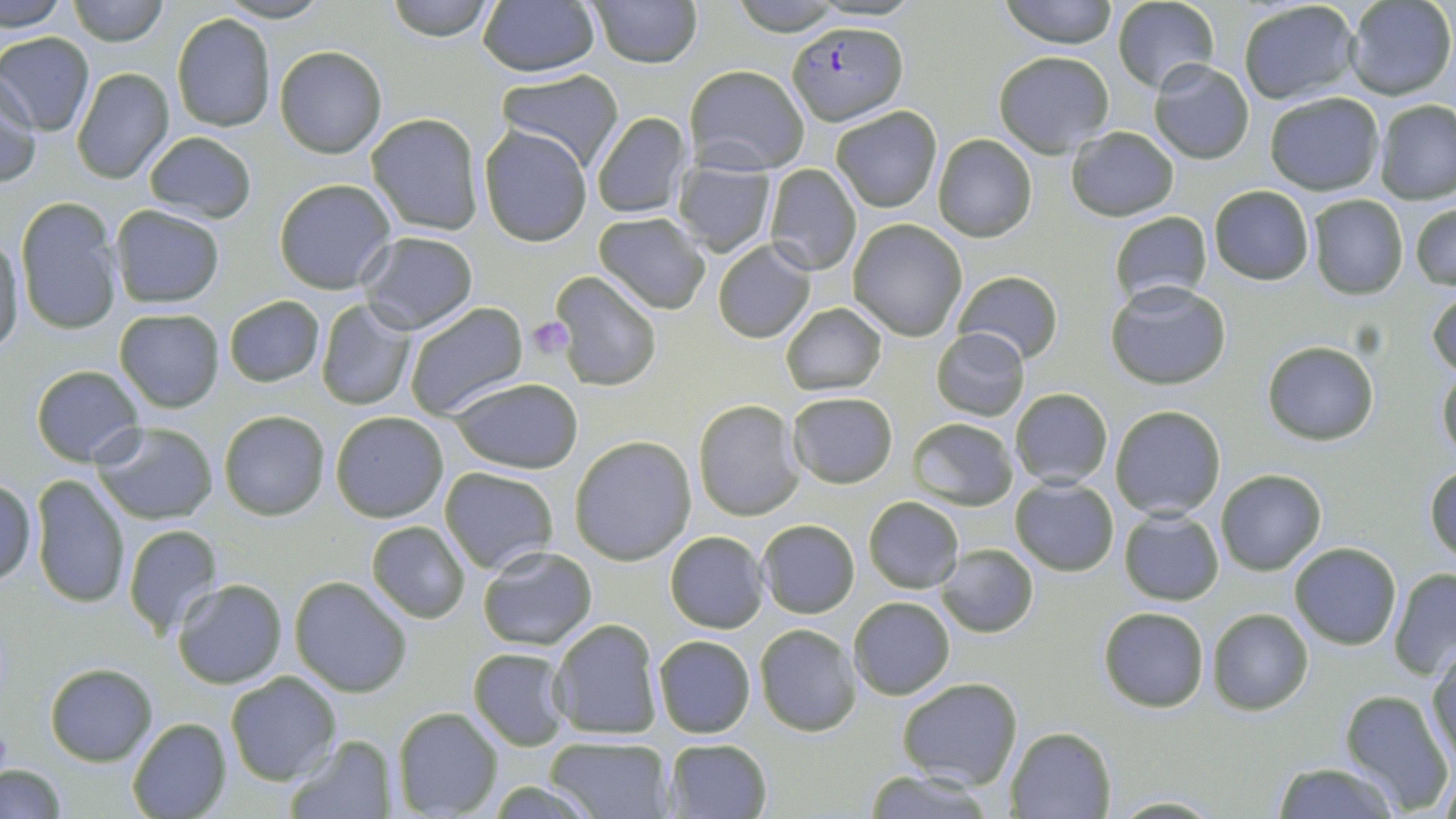

Summary:
  - Coordinate format: approximate bounding boxes as (x1, y1, x2, y2) in pixels
  - Platelet locations: (525, 317, 575, 359)
  - Plasmodium falciparum-infected red blood cell locations: (790, 20, 907, 123)
  - Uninfected red blood cell locations: (0, 0, 71, 33), (65, 0, 170, 46), (217, 0, 332, 23), (384, 0, 498, 41), (588, 0, 702, 68), (1000, 0, 1118, 49), (1344, 0, 1454, 100), (1112, 1, 1220, 95), (1237, 1, 1361, 106), (1361, 1, 1453, 203), (477, 2, 600, 77), (171, 12, 277, 132), (0, 32, 96, 136), (273, 45, 387, 158), (993, 51, 1115, 157), (1148, 59, 1254, 165), (684, 64, 809, 173), (71, 65, 174, 184), (498, 69, 624, 172), (1, 77, 40, 187), (1264, 91, 1384, 195), (1375, 99, 1456, 204), (831, 106, 941, 212), (590, 110, 691, 219), (366, 113, 486, 235), (479, 126, 593, 246), (1066, 127, 1178, 221), (143, 130, 257, 222), (932, 134, 1038, 242), (673, 159, 775, 257), (765, 165, 860, 275), (272, 178, 397, 294), (1208, 185, 1314, 285), (1306, 195, 1408, 298), (15, 198, 122, 334), (1410, 198, 1456, 291), (109, 204, 227, 309), (1109, 210, 1213, 307), (592, 211, 710, 313), (847, 220, 968, 341), (358, 230, 478, 333), (0, 231, 25, 360), (712, 241, 816, 343), (952, 269, 1064, 366), (551, 271, 663, 391), (1107, 281, 1231, 389), (1429, 288, 1456, 380), (224, 295, 324, 386), (315, 300, 415, 412), (402, 301, 528, 421), (780, 302, 886, 396), (115, 308, 224, 412), (931, 327, 1030, 422), (1262, 341, 1379, 444), (1437, 361, 1456, 465), (30, 363, 145, 466), (449, 376, 583, 475), (1008, 388, 1114, 488), (786, 392, 898, 488), (692, 398, 805, 521), (1109, 405, 1226, 519), (218, 409, 330, 521), (331, 411, 450, 522), (907, 418, 1018, 510), (92, 421, 220, 525), (569, 436, 696, 565), (1426, 464, 1456, 562), (439, 466, 559, 574), (1216, 468, 1327, 576), (29, 474, 131, 610), (1, 476, 37, 586), (1011, 477, 1118, 576), (864, 495, 964, 594), (1118, 510, 1225, 605), (756, 519, 860, 619), (366, 520, 470, 623), (121, 524, 224, 637), (664, 531, 768, 632), (1288, 543, 1401, 650), (938, 544, 1038, 638), (477, 545, 598, 650), (1388, 568, 1456, 677), (289, 576, 413, 697), (171, 577, 287, 688), (848, 596, 956, 699), (1098, 606, 1210, 712), (1207, 608, 1314, 714), (547, 618, 664, 741), (754, 623, 863, 735), (653, 635, 756, 739), (1427, 644, 1456, 768), (467, 648, 571, 750), (45, 662, 156, 764), (224, 670, 341, 785), (896, 676, 1023, 790), (1339, 690, 1452, 812), (391, 706, 502, 818), (125, 717, 232, 819), (1006, 726, 1116, 818), (286, 734, 397, 817), (545, 735, 673, 817), (664, 737, 773, 817), (1436, 756, 1455, 819), (1270, 763, 1399, 818), (1, 765, 65, 819), (860, 768, 996, 819), (1108, 794, 1224, 817)
  - Slide-level diagnosis: Plasmodium falciparum
  - Field of view: single
  - Image size: 1456×819 pixels
  - Stain: May-Grünwald-Giemsa
  - Magnification: 1000x
  - Modality: optical microscopy
  - Preparation: thin blood film